Comment on the morphology of the red blood cells.
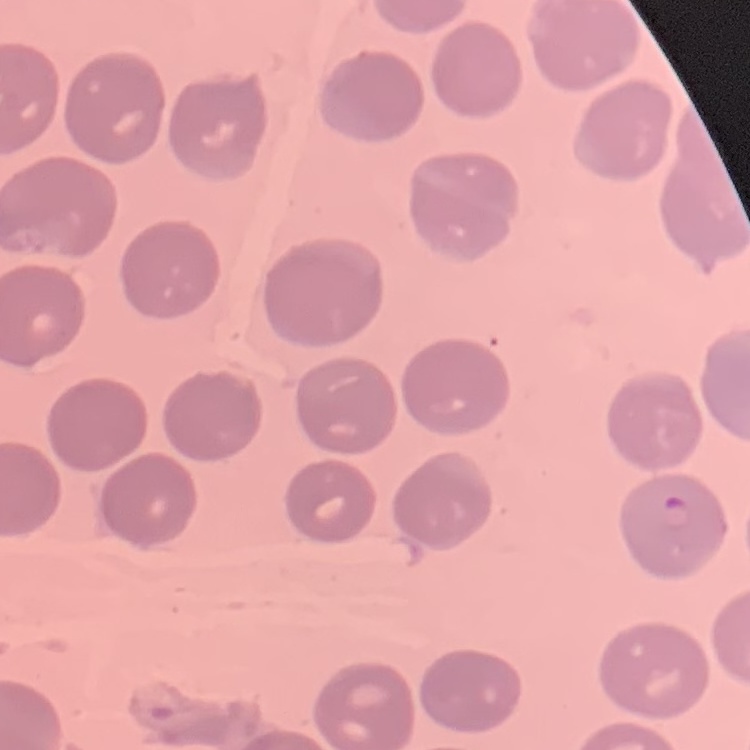
They show no rouleaux formation.

stain: Field's or Giemsa
image_type: square crop of a larger photomicrograph
preparation: thin peripheral smear